Report the malaria status of this cell.
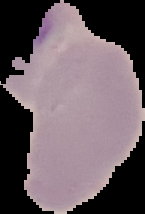

Uninfected.

preparation: thin blood smear
image_size: 145×214 pixels
image_type: cell region segmented out of the field of view; surrounding area masked to black